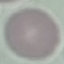
result = no malaria parasites seen
preparation = thin smear
stain = Giemsa
capture = smartphone camera at the microscope eyepiece
image type = cell patch, automatically extracted from a larger field of view and resized to 64 × 64 pixels